Point out each malaria parasite and each leukocyte.
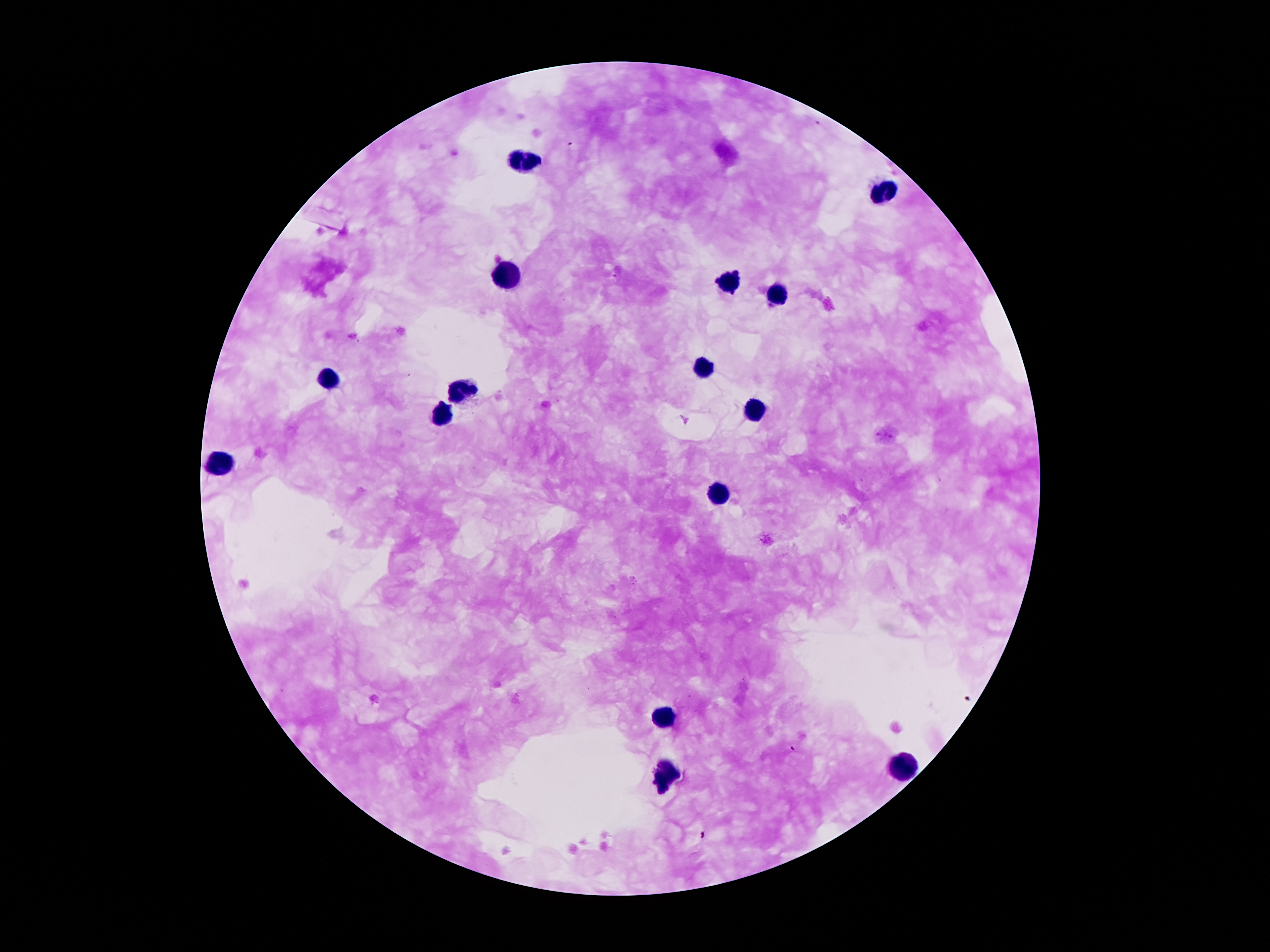
Approximate object centers, in pixels from the top-left corner.
Malaria parasites: (x=687, y=420).
Leukocytes: (x=526, y=161), (x=885, y=191), (x=506, y=276), (x=725, y=283), (x=776, y=294), (x=701, y=365), (x=330, y=382), (x=462, y=391), (x=750, y=410), (x=442, y=418), (x=217, y=463), (x=719, y=494), (x=661, y=717), (x=900, y=768), (x=667, y=771).

Photographed through the microscope eyepiece with a smartphone camera. Patient malaria status: infected with Plasmodium falciparum. Image is 1270×952 pixels. 100x magnification. Thick peripheral-blood smear. Giemsa-stained preparation. Single field of view.